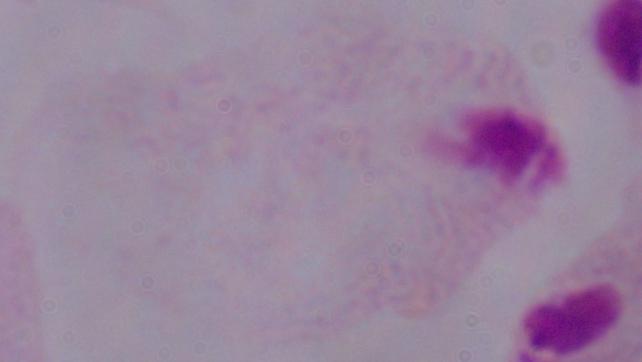

A trichomonad is shown. Captured at 1000x magnification. Micrograph.